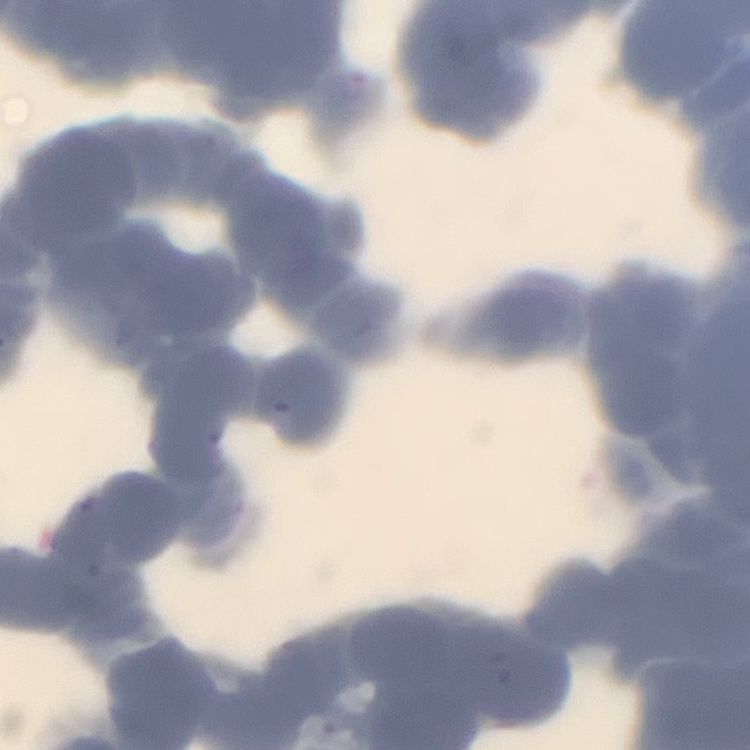
{
  "erythrocyte_morphology": "rouleaux formation",
  "stain": "Field's or Giemsa",
  "preparation": "thin blood smear",
  "image_type": "one tile cut from a larger photomicrograph"
}